Give the position of every leukocyte visible.
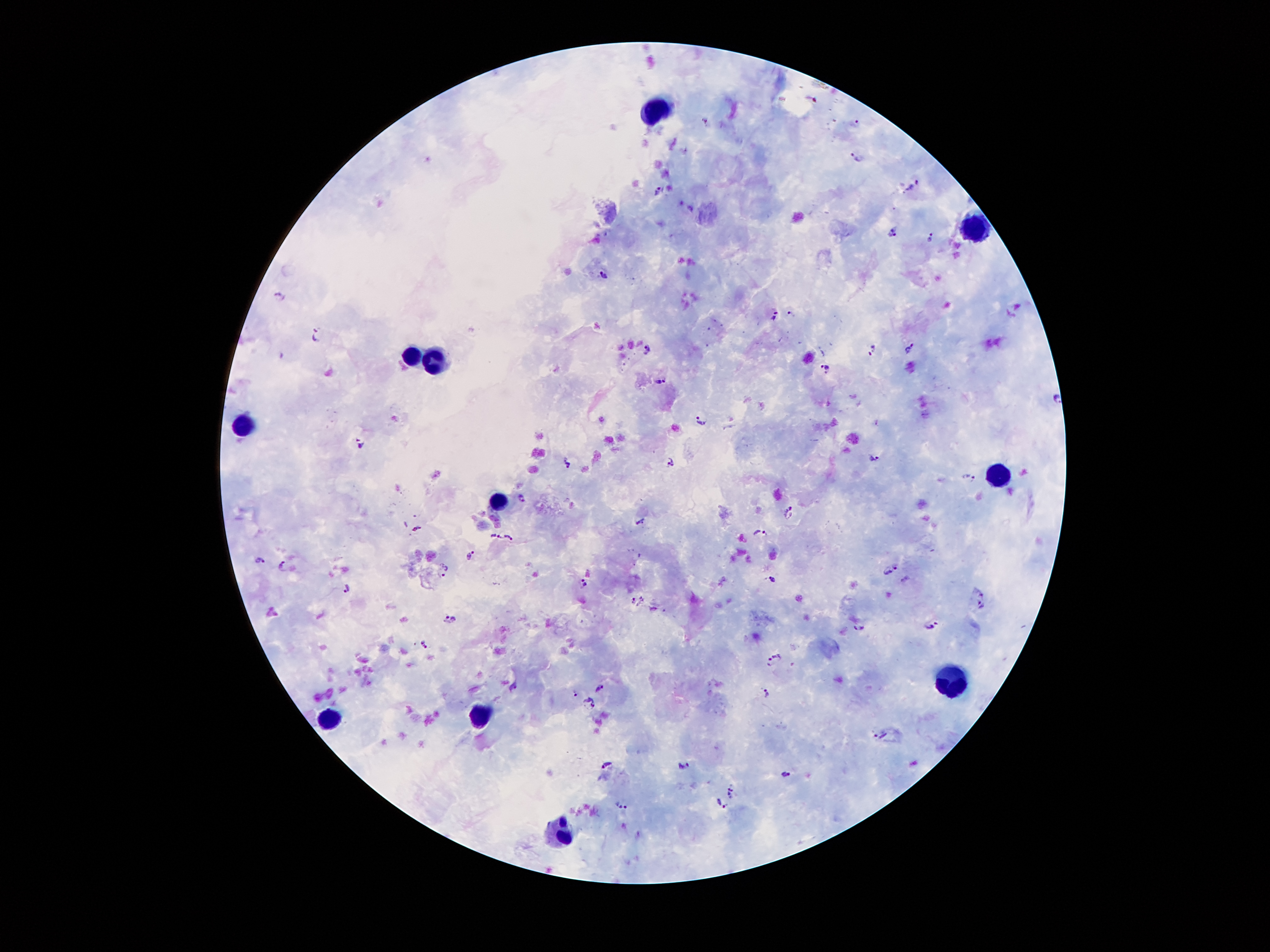
Approximate centers as [x, y] in pixels.
Leukocytes: [657, 107], [973, 232], [411, 356], [434, 361], [238, 424], [1003, 477], [497, 500], [951, 679], [481, 714], [327, 719], [556, 833].

Summary:
  - Malaria parasite locations: [856, 122], [710, 123], [854, 160], [914, 186], [657, 191], [894, 233], [930, 234], [605, 276], [281, 297], [775, 314], [791, 316], [315, 337], [648, 348], [910, 350], [872, 352], [825, 368], [660, 381], [1057, 400], [702, 421], [361, 441], [875, 457], [567, 463], [672, 463], [969, 479], [521, 497], [790, 512], [641, 522], [416, 527], [762, 533], [496, 537], [508, 537], [472, 556], [257, 560], [284, 565], [445, 569], [891, 571], [772, 578], [906, 579], [584, 584], [348, 589], [982, 592], [630, 599], [642, 601], [651, 610], [980, 610], [449, 620], [859, 627], [932, 627], [424, 644], [775, 660], [514, 685], [599, 687], [572, 692], [767, 693], [590, 702], [880, 734], [608, 764], [684, 766], [785, 774], [732, 788], [621, 804], [722, 804]
  - Field of view: one from this slide
  - Preparation: thick blood film
  - Image size: 1270×952 pixels
  - Magnification: 100x
  - Capture: smartphone camera through the microscope eyepiece
  - Stain: Giemsa
  - Patient malaria status: infected with Plasmodium falciparum